State which parasite is depicted.
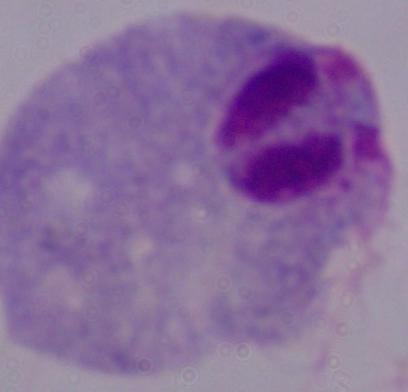
This is a trichomonad.

{
  "modality": "photomicrograph",
  "magnification": "1000x"
}